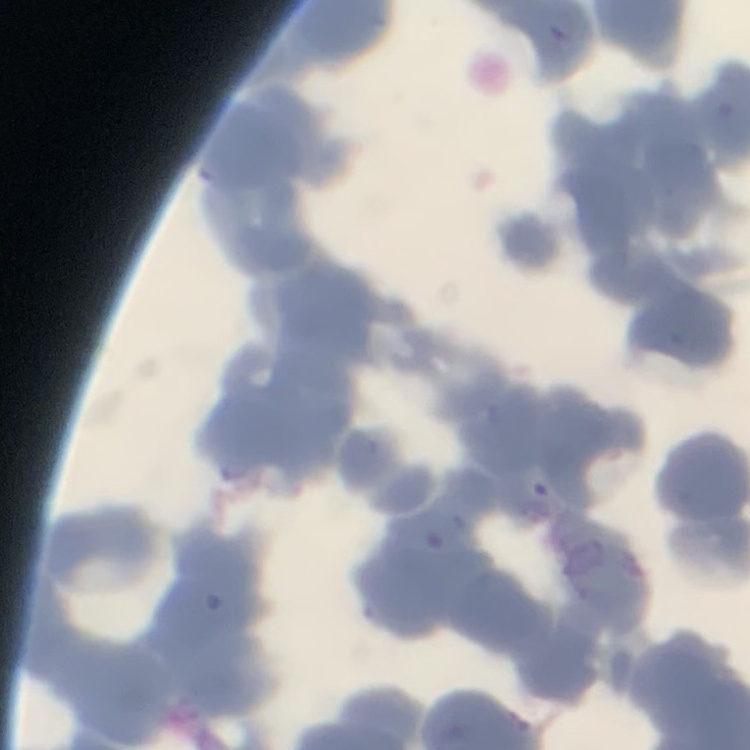
red blood cell morphology = rouleaux formation
stain = Field's or Giemsa
preparation = thin blood film
image type = one tile cut from a larger photomicrograph